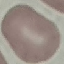
result = no malaria parasites seen
stain = Giemsa
preparation = thin blood film
image type = cell patch, automatically extracted from a larger field of view and resized to 64 × 64 pixels
capture = smartphone through the microscope eyepiece